Name the parasite shown.
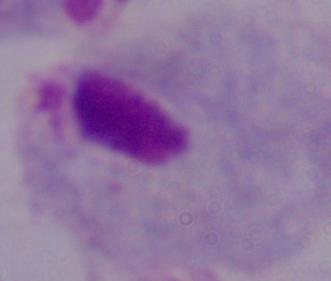
A trichomonad.

Captured at 1000x magnification. Micrograph.